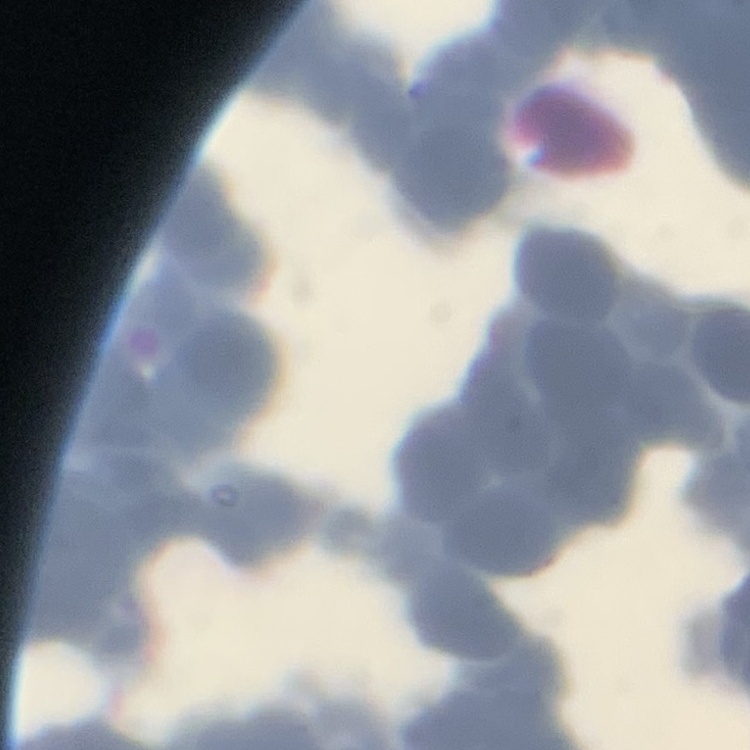

Summary:
  - Red blood cell morphology: rouleaux formation
  - Stain: Field's or Giemsa
  - Image type: one tile cut from a larger photomicrograph
  - Preparation: thin peripheral smear